Assess the morphology of the erythrocytes.
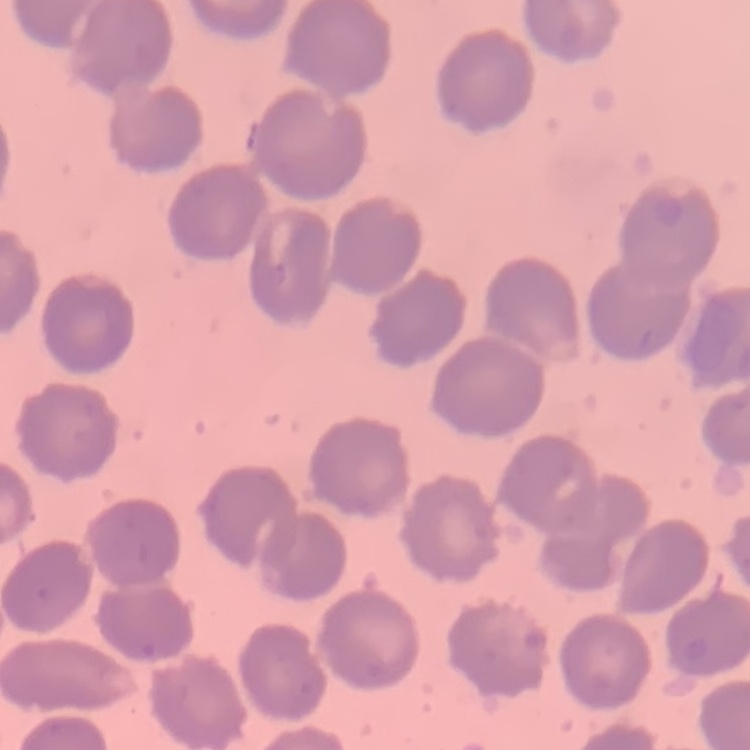
No rouleaux formation.

image_type: one tile cut from a larger photomicrograph
stain: Field's or Giemsa
preparation: thin peripheral smear